Outline each blood parasite and name the species.
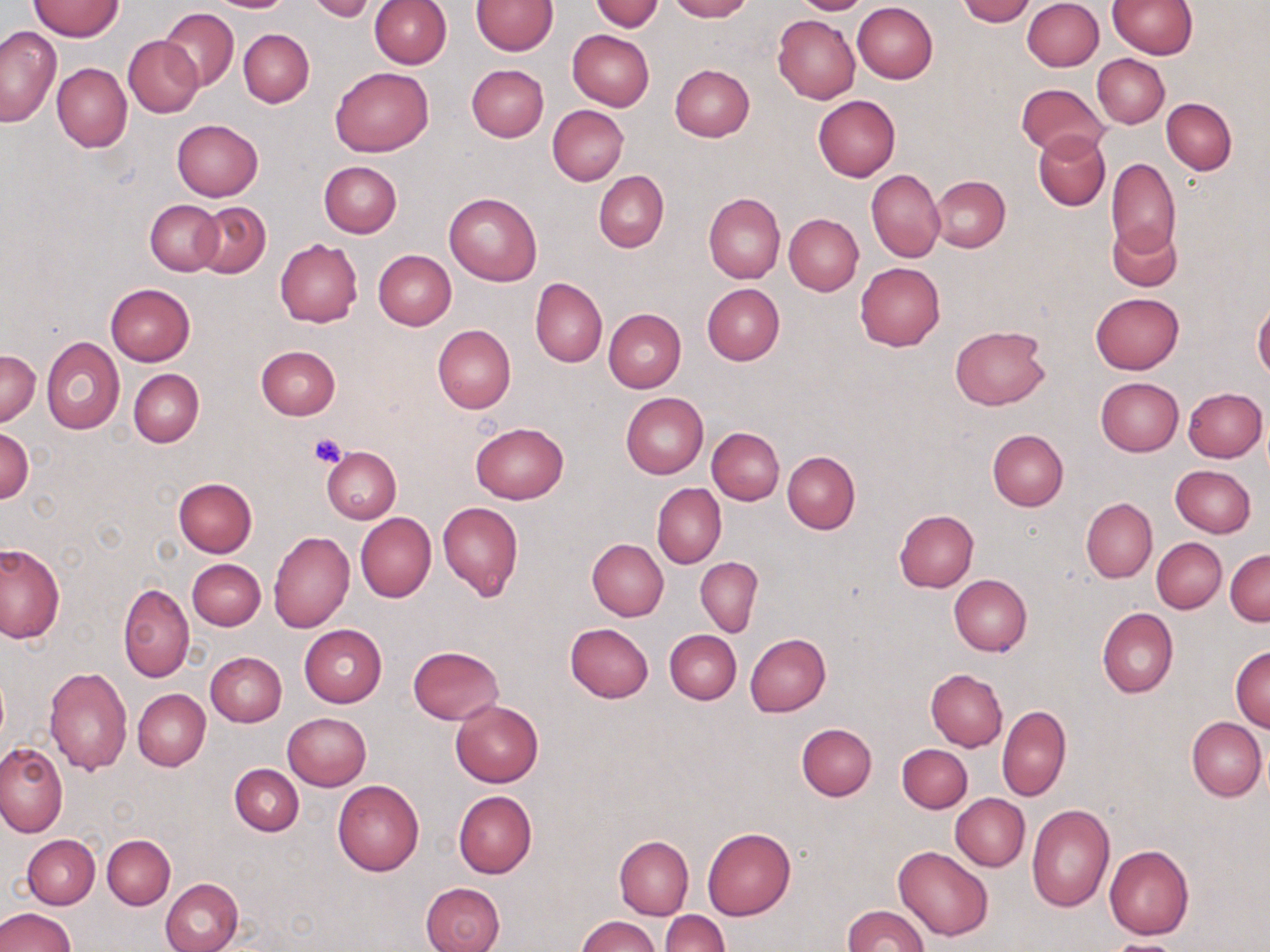

No blood parasites seen.

Approximate bounding boxes as (x1, y1, x2, y2) in pixels. Uninfected red blood cell locations: (206, 0, 293, 12), (592, 0, 662, 32), (665, 0, 751, 21), (790, 0, 871, 14), (958, 0, 1034, 25), (1022, 0, 1103, 71), (1108, 0, 1196, 58), (27, 1, 125, 41), (306, 1, 379, 22), (369, 1, 450, 69), (473, 1, 557, 55), (852, 2, 938, 83), (159, 7, 239, 92), (773, 15, 860, 104), (0, 26, 61, 126), (239, 29, 314, 108), (566, 29, 655, 111), (124, 35, 202, 117), (1092, 55, 1169, 127), (52, 63, 132, 151), (466, 64, 548, 142), (670, 64, 754, 142), (330, 67, 432, 156), (1017, 83, 1111, 158), (813, 95, 901, 181), (1162, 98, 1237, 174), (547, 104, 629, 185), (172, 119, 263, 202), (1034, 130, 1111, 211), (1107, 157, 1180, 259), (319, 162, 402, 238), (867, 170, 945, 262), (593, 172, 668, 252), (932, 176, 1009, 251), (444, 192, 542, 286), (703, 193, 785, 283), (146, 199, 223, 276), (193, 201, 271, 278), (783, 213, 863, 295), (1107, 221, 1181, 290), (275, 239, 362, 327), (374, 250, 456, 330), (855, 262, 946, 351), (530, 276, 606, 367), (104, 282, 196, 366), (702, 283, 784, 365), (1090, 293, 1185, 374), (1253, 300, 1270, 380), (604, 309, 686, 393), (432, 324, 516, 414), (950, 325, 1050, 409), (41, 336, 123, 434), (256, 345, 341, 419), (1, 351, 40, 425), (129, 369, 203, 447), (1096, 377, 1183, 455), (1184, 388, 1267, 462), (1181, 389, 1261, 537), (620, 392, 708, 478), (470, 423, 568, 504), (1, 426, 34, 503), (707, 427, 784, 504), (987, 430, 1068, 511), (321, 446, 401, 524), (782, 451, 860, 535), (1170, 465, 1256, 537), (173, 478, 257, 557), (653, 484, 726, 569), (1082, 498, 1157, 583), (437, 501, 523, 602), (894, 510, 979, 593), (355, 512, 436, 602), (268, 531, 354, 633), (587, 538, 669, 620), (1152, 538, 1226, 613), (0, 543, 64, 643), (1226, 549, 1270, 625), (695, 557, 763, 638), (187, 559, 265, 630), (948, 574, 1032, 655), (118, 583, 193, 682), (1097, 607, 1177, 698), (564, 622, 653, 702), (299, 624, 387, 707), (665, 630, 741, 704), (745, 633, 831, 716), (408, 646, 504, 724), (1230, 646, 1270, 731), (205, 651, 287, 726), (43, 667, 132, 775), (925, 670, 1007, 751), (132, 689, 209, 770), (451, 698, 543, 787), (997, 705, 1072, 801), (284, 712, 371, 790), (1186, 717, 1266, 800), (797, 723, 877, 801), (897, 743, 972, 813), (0, 744, 67, 836), (229, 764, 304, 835), (333, 780, 424, 876), (454, 792, 537, 878), (950, 793, 1030, 871), (1026, 804, 1115, 913), (702, 827, 795, 920), (102, 833, 175, 909), (22, 834, 100, 908), (615, 836, 693, 919), (894, 845, 993, 941), (1105, 845, 1193, 940), (161, 877, 242, 952), (421, 882, 506, 952), (842, 905, 927, 952), (0, 906, 76, 952), (661, 911, 728, 952), (577, 915, 660, 952), (1104, 938, 1185, 952). Platelet locations: (308, 431, 348, 468). Slide-level diagnosis: negative for blood parasites. May-Grünwald-Giemsa stain. Image is 1270×952 pixels. Thin blood film. Light microscopy. Single field of view. Captured at 1000x magnification.